Name the parasite shown.
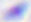
Toxoplasma gondii.

Summary:
  - Magnification: 400x
  - Modality: photomicrograph